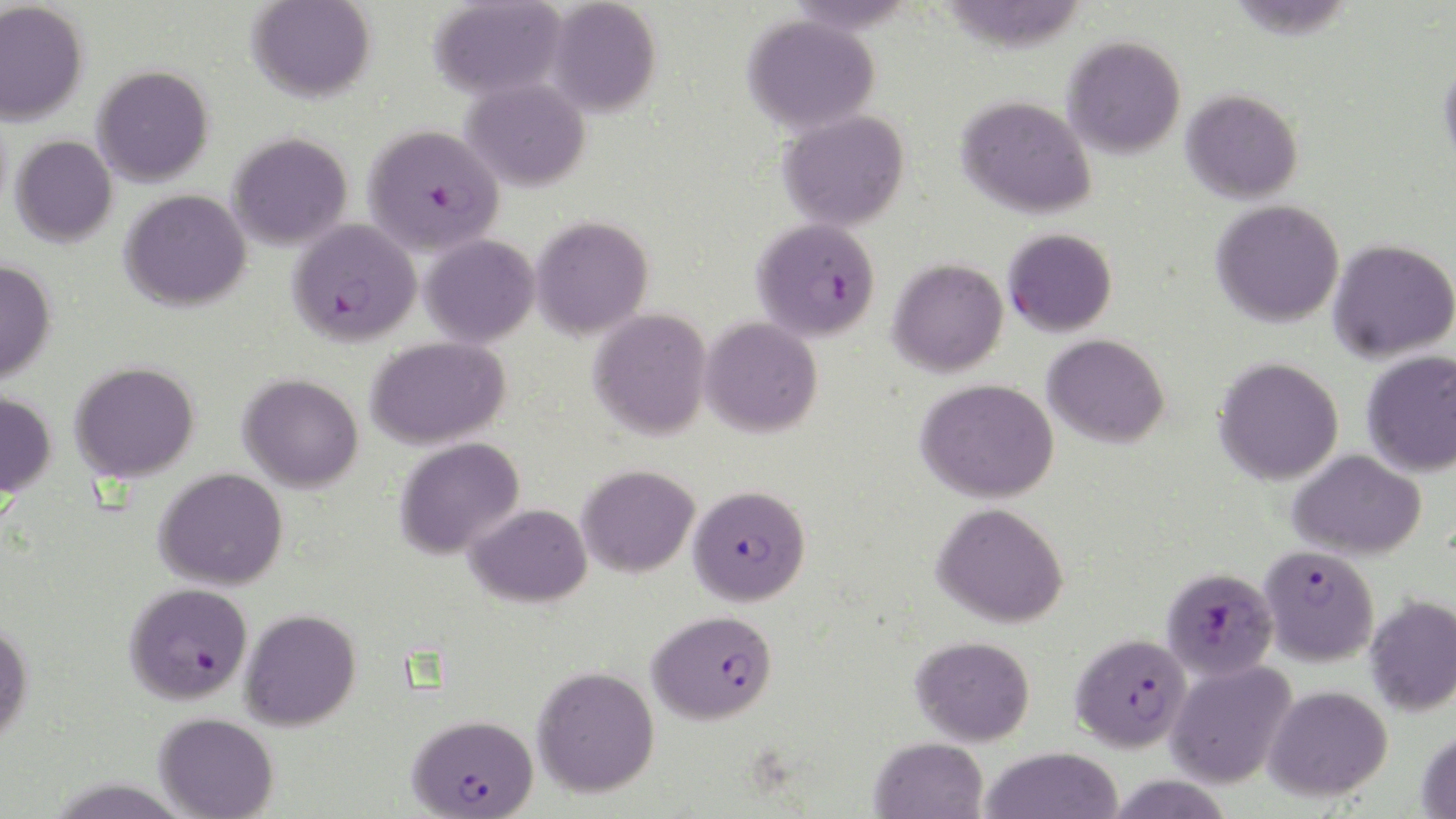 Approximate bounding boxes as (x1, y1, x2, y2) in pixels. Plasmodium falciparum-infected red blood cell locations: (362, 125, 504, 257), (752, 217, 880, 341), (287, 219, 422, 347), (688, 484, 811, 606), (1258, 544, 1379, 666), (1161, 567, 1279, 681), (124, 581, 252, 704), (647, 610, 778, 724), (1070, 632, 1191, 753), (406, 715, 539, 819). Uninfected red blood cell locations: (247, 0, 375, 103), (428, 0, 567, 100), (545, 0, 661, 117), (0, 2, 88, 125), (742, 14, 880, 135), (1063, 36, 1186, 159), (1439, 55, 1456, 175), (92, 65, 213, 186), (460, 78, 590, 191), (1181, 88, 1303, 203), (957, 95, 1096, 219), (777, 109, 910, 231), (227, 132, 353, 251), (11, 136, 117, 247), (120, 190, 251, 312), (1211, 200, 1345, 328), (530, 216, 653, 339), (1003, 228, 1117, 337), (420, 235, 539, 347), (1328, 239, 1456, 362), (887, 258, 1008, 377), (0, 260, 56, 384), (589, 308, 711, 440), (699, 317, 823, 437), (1043, 334, 1170, 448), (366, 336, 510, 450), (1362, 350, 1456, 476), (1213, 356, 1345, 485), (70, 361, 199, 483), (238, 374, 363, 492), (916, 378, 1060, 503), (0, 389, 56, 499), (394, 437, 525, 559), (1289, 450, 1427, 559), (577, 465, 699, 578), (154, 467, 288, 591), (932, 502, 1069, 628), (465, 503, 592, 608), (1364, 594, 1456, 717), (240, 608, 361, 731), (0, 619, 34, 745), (910, 635, 1035, 745), (1165, 659, 1298, 789), (531, 665, 660, 797), (1262, 684, 1393, 801), (153, 711, 279, 819), (1416, 728, 1456, 818), (869, 737, 988, 819), (980, 747, 1123, 819). Slide-level diagnosis: Plasmodium falciparum. Light microscopy. Thin blood film. Image is 1456×819 pixels. Single field of view. May-Grünwald-Giemsa stain. 1000x magnification.